Identify the parasite.
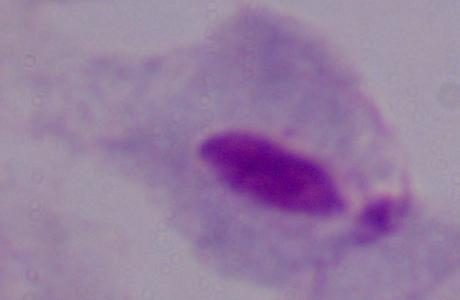

A trichomonad.

Summary:
  - Modality: micrograph
  - Magnification: 1000x